Identify the cell.
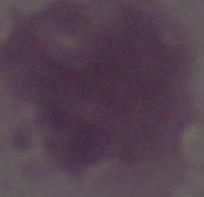
An erythrocyte.

magnification: 1000x
modality: photomicrograph